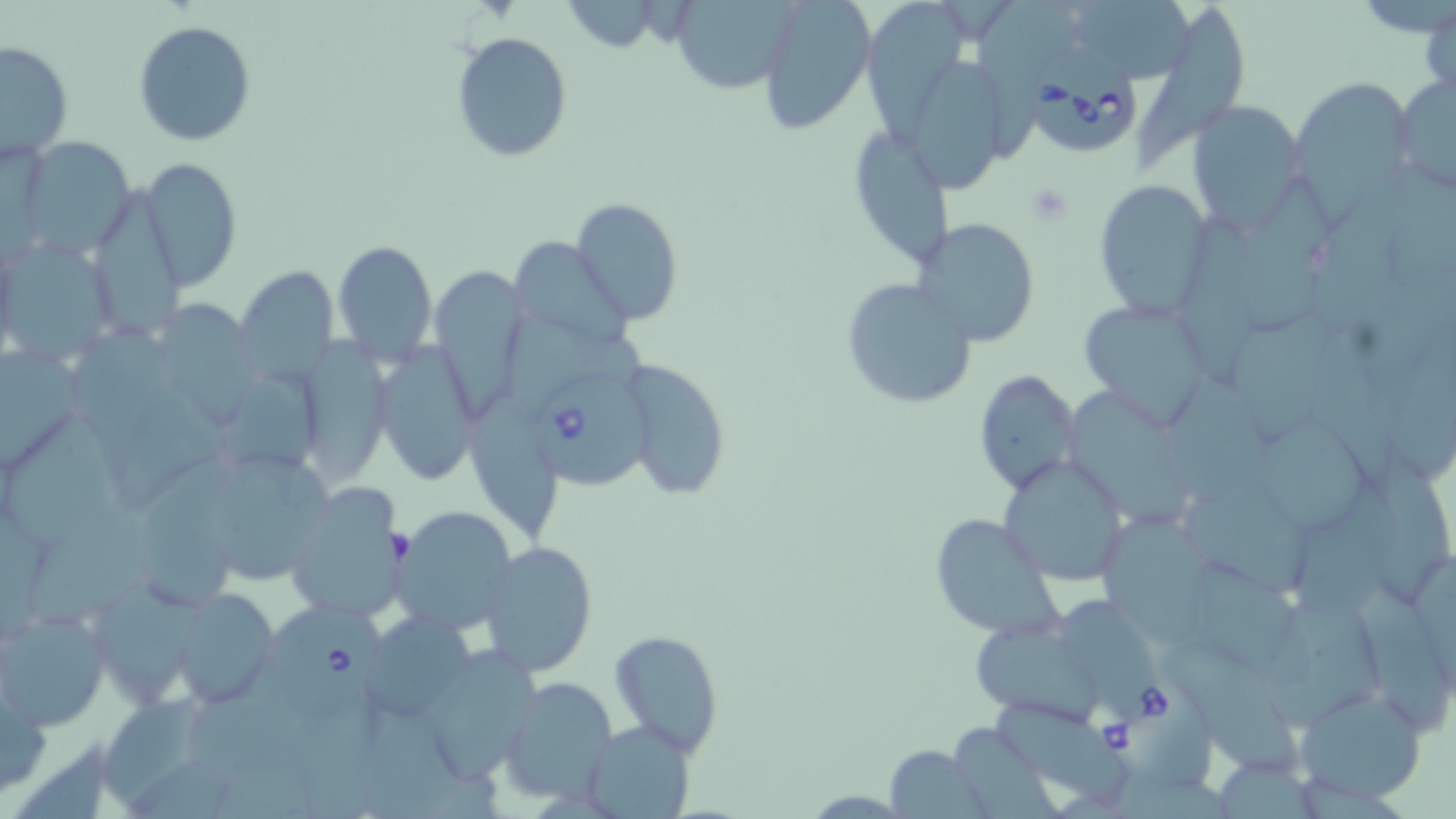
{
  "slide_level_diagnosis": "Babesia divergens",
  "stain": "May-Grünwald-Giemsa",
  "field_of_view": "single",
  "image_size": "1456×819 pixels",
  "platelet_locations": "approximate bounding boxes as (x1,y1)-(x2,y2) corner pairs in pixels: (1023,183)-(1076,226)",
  "magnification": "1000x",
  "preparation": "thin blood film",
  "uninfected_red_blood_cell_locations": "approximate bounding boxes as (x1,y1)-(x2,y2) corner pairs in pixels: (669,0)-(799,94), (758,0)-(876,134), (986,0)-(1072,157), (1065,0)-(1197,86), (1136,0)-(1251,166), (859,4)-(966,148), (132,19)-(256,146), (449,30)-(574,162), (1,38)-(74,163), (911,55)-(1006,195), (1392,70)-(1456,196), (1294,80)-(1419,206), (1189,100)-(1307,228), (858,126)-(953,272), (18,139)-(134,258), (141,160)-(241,292), (1246,170)-(1335,330), (1091,177)-(1214,319), (88,190)-(187,337), (572,197)-(683,324), (1310,197)-(1403,327), (1176,212)-(1264,371), (918,218)-(1040,346), (509,237)-(627,349), (332,239)-(438,366), (1,243)-(123,357), (233,265)-(339,383), (431,269)-(527,421), (840,279)-(976,410), (1074,294)-(1217,425), (158,296)-(253,418), (502,312)-(648,409), (1233,316)-(1339,431), (75,323)-(173,450), (298,330)-(404,487), (372,343)-(482,486), (0,346)-(83,471), (620,358)-(732,503), (973,369)-(1081,495), (225,373)-(318,469), (116,382)-(230,506), (1177,386)-(1274,510), (1064,395)-(1191,525), (9,418)-(125,548), (1261,420)-(1367,532), (214,445)-(339,584), (1365,451)-(1454,604), (997,457)-(1130,586), (141,469)-(240,605), (1299,478)-(1396,625), (285,482)-(410,624), (1183,483)-(1314,592), (22,503)-(156,626), (392,503)-(516,634), (928,513)-(1061,637), (1106,518)-(1208,644), (480,541)-(597,677), (1189,562)-(1301,676), (1359,580)-(1453,739), (91,582)-(214,705), (173,588)-(278,707), (1058,595)-(1149,700), (1,605)-(111,732), (1274,608)-(1394,732), (371,620)-(479,720), (972,622)-(1099,724), (609,628)-(724,755), (1168,637)-(1299,770), (419,647)-(549,784), (498,676)-(619,805), (0,677)-(47,800), (1293,687)-(1428,804), (105,696)-(203,801), (995,701)-(1131,808), (356,710)-(468,819), (584,718)-(696,819), (887,744)-(986,815)",
  "modality": "light microscopy",
  "babesia_divergens_infected_red_blood_cell_locations": "approximate bounding boxes as (x1,y1)-(x2,y2) corner pairs in pixels: (1030,45)-(1138,154), (535,369)-(652,490), (266,601)-(389,723), (1082,660)-(1219,786)"
}